State the preparation type.
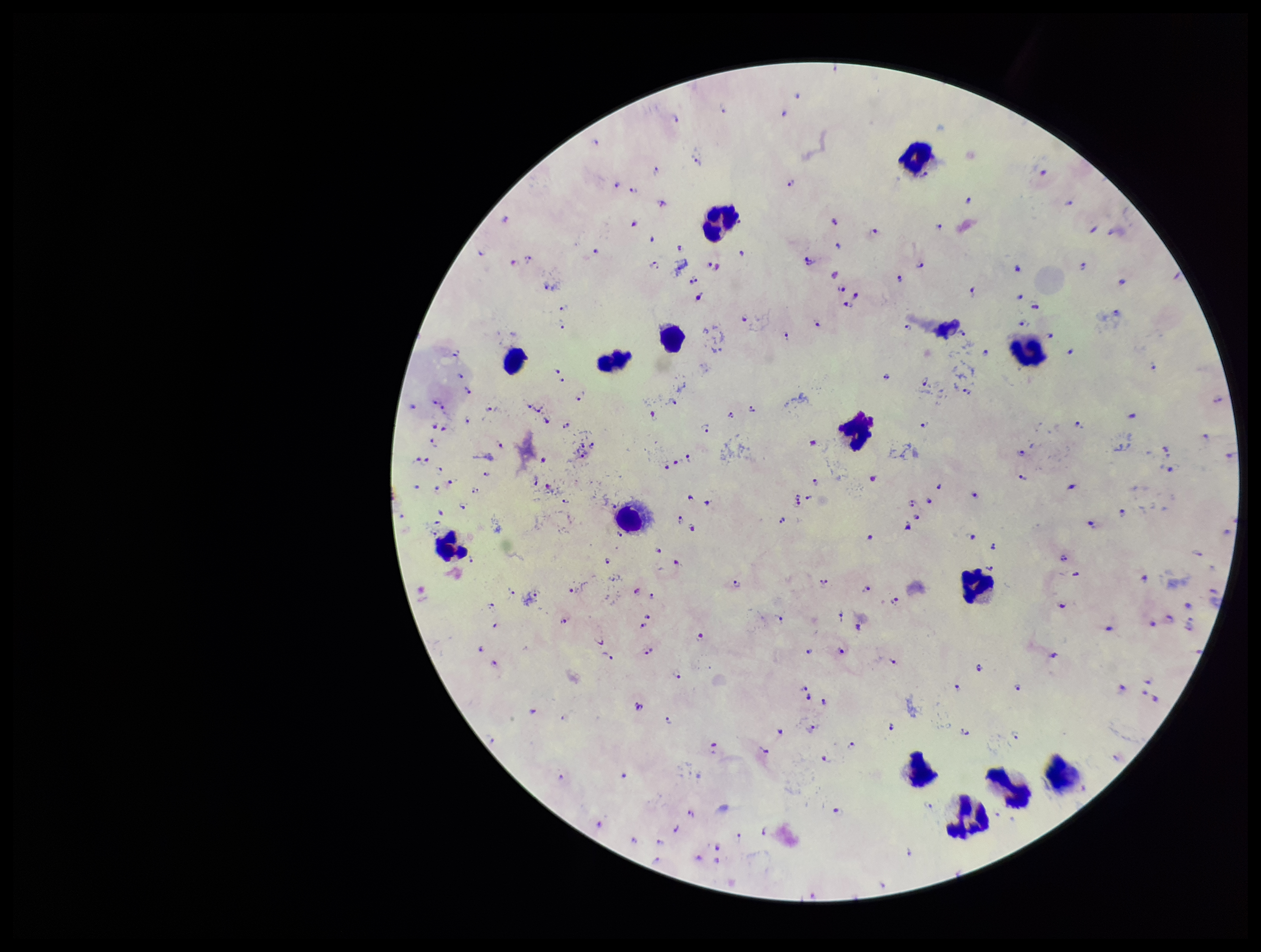
Thick.

stain = Giemsa
field of view = single
capture = smartphone photograph through the microscope eyepiece
leukocyte count = 15
image size = 1261×952 pixels
parasite count = 119
species reported for this patient = Plasmodium falciparum
patient malaria status = infected
Plasmodium parasites = identified